Report the malaria status of this cell.
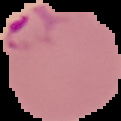

Parasitized.

{
  "image_size": "121×121 pixels",
  "image_type": "cell region segmented out of the field of view; surrounding area masked to black",
  "preparation": "thin blood smear"
}